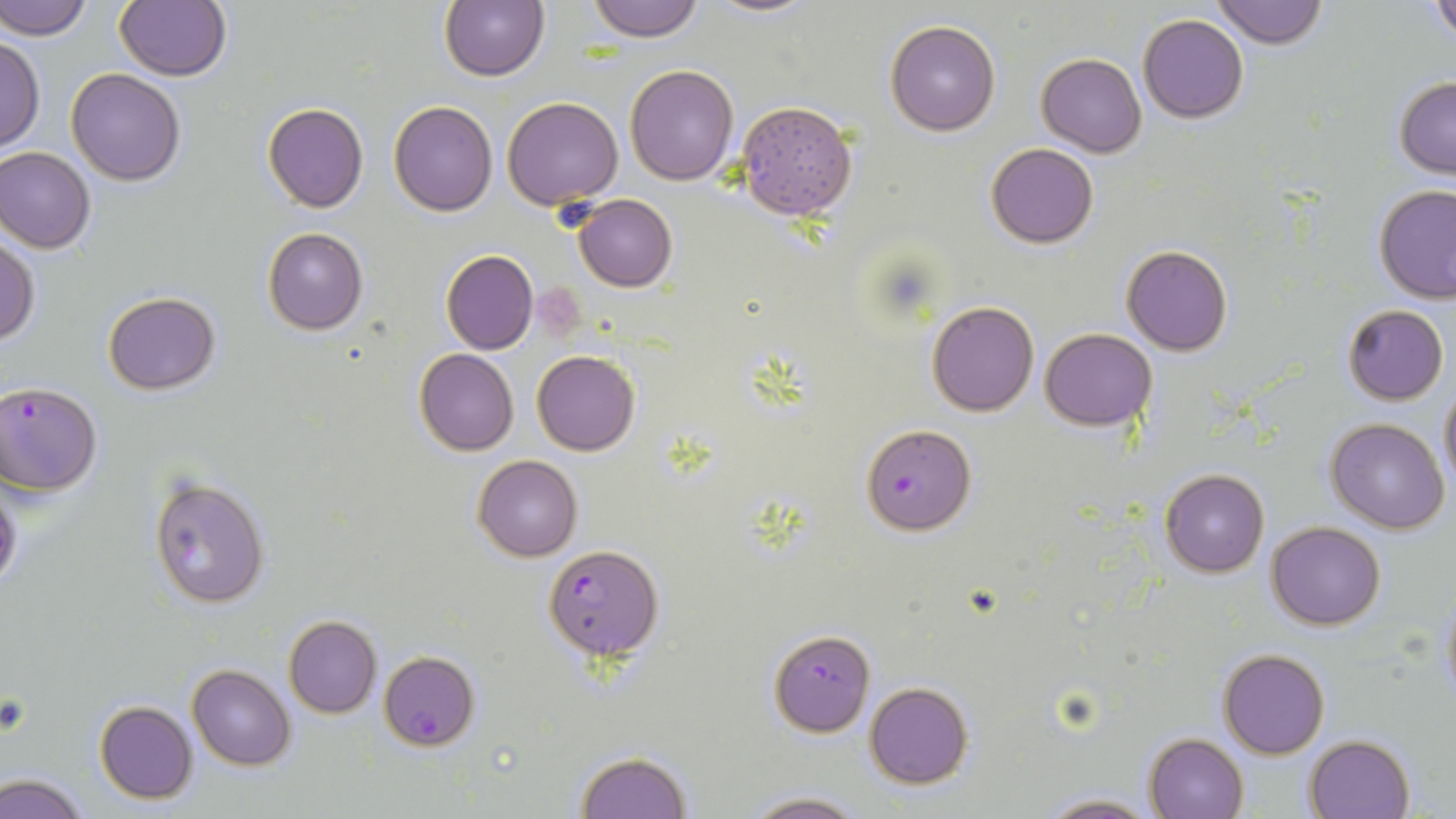

slide_level_diagnosis: Plasmodium falciparum
image_size: 1456×819 pixels
uninfected_red_blood_cell_locations: 'approximate bounding boxes as [x1, y1, x2, y2] in pixels: [1, 0, 93, 41], [116, 0, 231, 81], [439, 0, 550, 82], [584, 0, 707, 42], [694, 0, 824, 17], [1212, 0, 1328, 47], [1427, 0, 1456, 43], [1138, 14, 1250, 123], [884, 21, 1000, 135], [0, 34, 44, 154], [1037, 53, 1146, 156], [625, 63, 740, 185], [66, 67, 187, 184], [1393, 75, 1456, 179], [502, 97, 622, 208], [734, 99, 858, 221], [389, 101, 497, 217], [262, 102, 368, 214], [986, 143, 1097, 249], [1, 146, 96, 253], [1375, 185, 1456, 302], [571, 194, 677, 292], [262, 227, 367, 336], [0, 237, 39, 345], [1120, 244, 1233, 356], [441, 249, 538, 355], [103, 291, 221, 395], [928, 301, 1038, 416], [1342, 304, 1449, 405], [1039, 327, 1158, 431], [414, 349, 518, 455], [533, 351, 639, 456], [1438, 379, 1456, 494], [1326, 419, 1449, 533], [472, 455, 583, 562], [1159, 469, 1269, 578], [147, 475, 270, 610], [0, 480, 21, 594], [1266, 521, 1386, 630], [1438, 585, 1456, 707], [284, 615, 381, 718], [1218, 647, 1330, 759], [187, 664, 296, 770], [863, 681, 974, 788], [95, 700, 199, 803], [1144, 732, 1248, 819], [1304, 734, 1414, 819], [573, 750, 691, 819], [0, 772, 89, 818], [740, 792, 869, 819], [1033, 793, 1164, 819]'
stain: May-Grünwald-Giemsa
field_of_view: one of a larger specimen
modality: light microscopy
plasmodium_falciparum_infected_red_blood_cell_locations: 'approximate bounding boxes as [x1, y1, x2, y2] in pixels: [1, 382, 103, 496], [860, 424, 975, 535], [544, 543, 661, 660], [768, 629, 875, 736], [378, 650, 481, 750]'
magnification: 1000x
preparation: thin blood film